Describe the morphology of the erythrocytes.
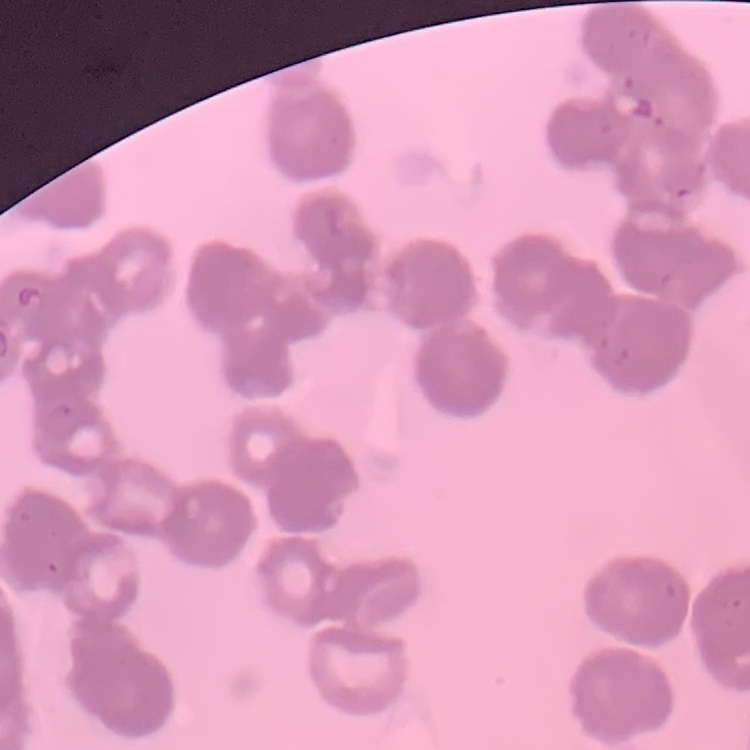
They show rouleaux formation.

Stained with either Field's or Giemsa. One tile cut from a larger photomicrograph. Thin peripheral smear.